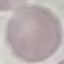

Result: no malaria parasites detected. Cell patch, automatically extracted from a larger field of view and resized to 64 × 64 pixels. Photographed with a smartphone camera at the microscope eyepiece. Thin blood film. Giemsa-stained preparation.